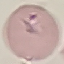

Malaria status: parasitized. Giemsa-stained preparation. Automatically extracted cell patch, resized to 64 × 64 pixels. Thin blood film. Acquired by smartphone through the microscope eyepiece.